Identify the parasite.
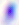

Toxoplasma gondii.

Summary:
  - Modality: micrograph
  - Magnification: 400x